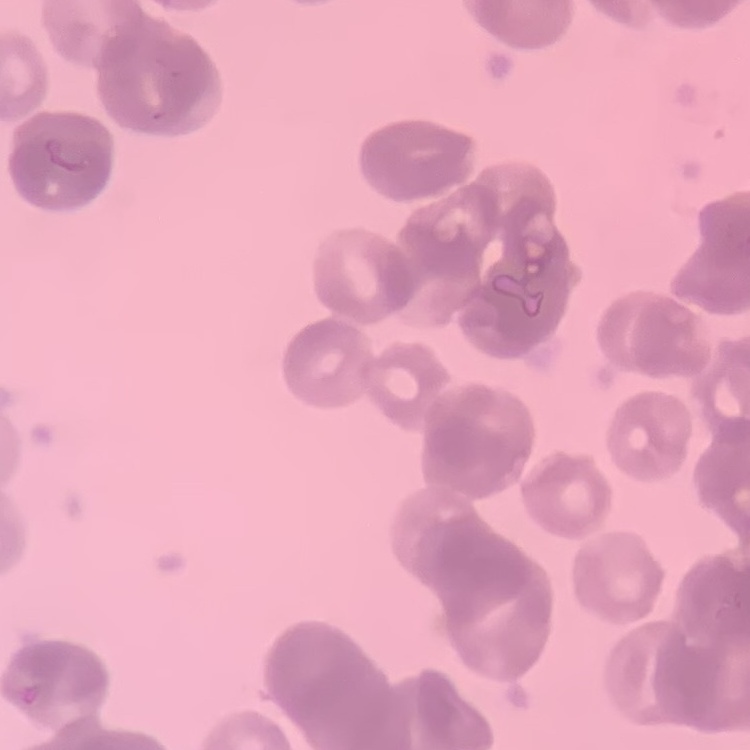

Summary:
  - Red blood cell morphology: rouleaux formation
  - Stain: Field's or Giemsa
  - Preparation: thin blood smear
  - Image type: square crop of a larger photomicrograph